Identify the parasite.
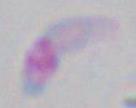

This is Toxoplasma gondii.

Captured at 1000x magnification. Micrograph.